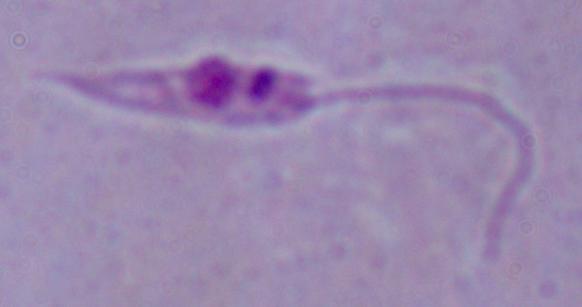

modality = micrograph
magnification = 1000x
identification = Leishmania